Report the malaria status of this cell.
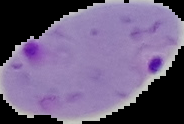
Parasitized.

image type = segmented cell region on a black background
preparation = thin blood film
image size = 184×124 pixels